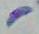

modality = photomicrograph
magnification = 1000x
identification = Toxoplasma gondii